Find the cells and give the type of each one.
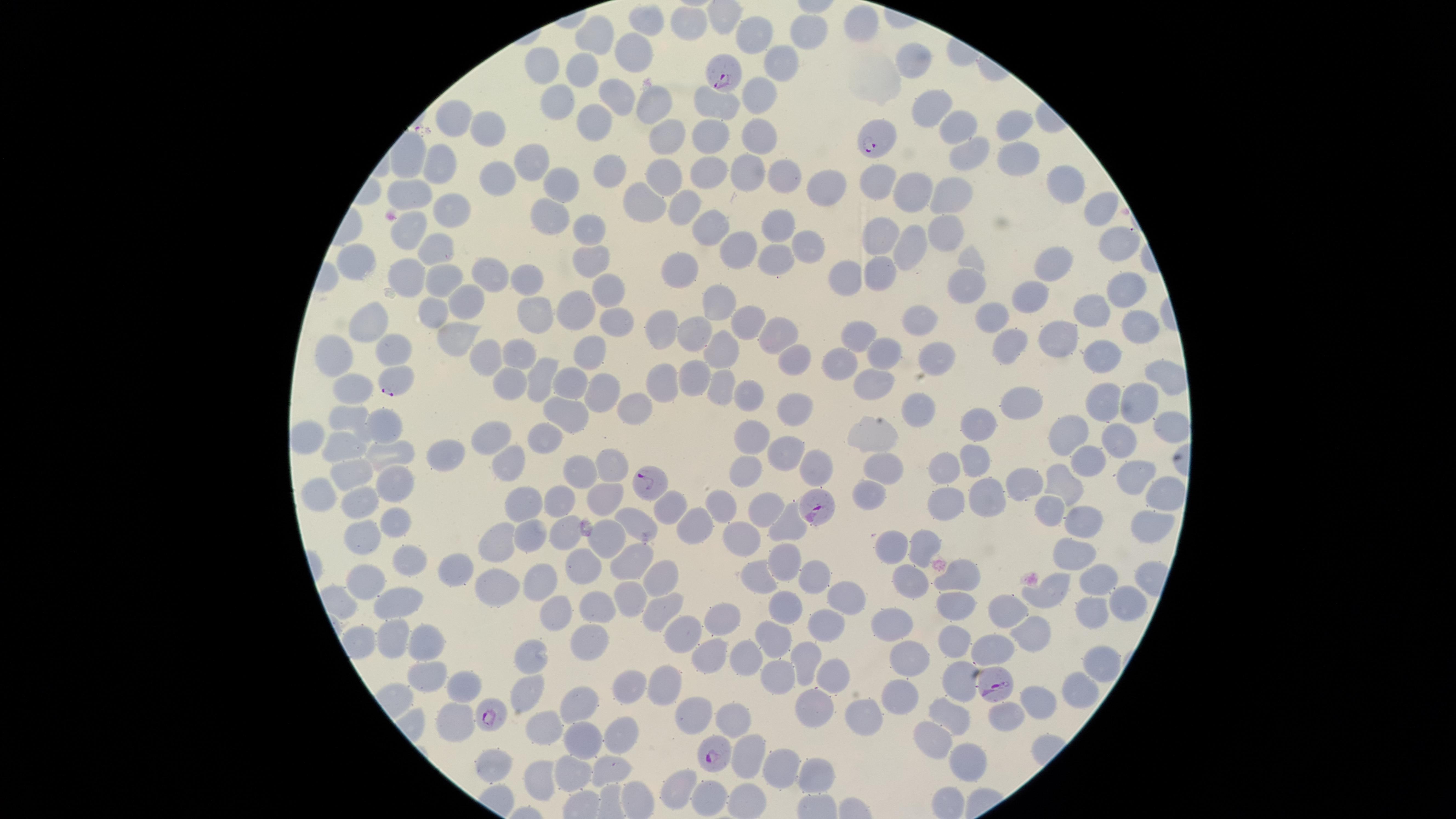

Approximate marker points, in pixels from the top-left corner.
Parasitized red blood cells: (x=728, y=77), (x=878, y=142), (x=397, y=380), (x=651, y=481), (x=812, y=506), (x=991, y=689), (x=489, y=715), (x=710, y=750).
Uninfected red blood cells: (x=646, y=23), (x=685, y=25), (x=861, y=27), (x=810, y=30), (x=755, y=32), (x=595, y=35), (x=633, y=55), (x=911, y=61), (x=779, y=65), (x=543, y=68), (x=582, y=72), (x=616, y=90), (x=756, y=92), (x=558, y=100), (x=712, y=102), (x=651, y=106), (x=926, y=108), (x=456, y=120), (x=596, y=122), (x=490, y=123), (x=958, y=129), (x=1020, y=129), (x=762, y=130), (x=665, y=132), (x=715, y=132), (x=968, y=153), (x=1019, y=156), (x=410, y=159), (x=536, y=159), (x=442, y=166), (x=611, y=167), (x=712, y=169), (x=741, y=171), (x=662, y=172), (x=781, y=172), (x=492, y=175), (x=875, y=177), (x=1058, y=181), (x=817, y=185), (x=565, y=186), (x=911, y=188), (x=413, y=192), (x=947, y=197), (x=644, y=199), (x=686, y=203), (x=1095, y=207), (x=452, y=208), (x=545, y=214), (x=588, y=224), (x=781, y=224), (x=708, y=229), (x=879, y=233), (x=410, y=234), (x=945, y=236), (x=435, y=245), (x=906, y=245), (x=740, y=248), (x=803, y=249), (x=1119, y=249), (x=586, y=256), (x=775, y=258), (x=361, y=260), (x=1054, y=262), (x=677, y=264), (x=880, y=265), (x=403, y=272), (x=441, y=273), (x=491, y=273), (x=523, y=275), (x=845, y=275), (x=962, y=285), (x=610, y=286), (x=1121, y=289), (x=1032, y=298), (x=459, y=301), (x=716, y=304), (x=1092, y=308), (x=572, y=309), (x=432, y=312), (x=536, y=316), (x=994, y=318), (x=1138, y=319), (x=619, y=320), (x=374, y=321), (x=917, y=321), (x=741, y=323), (x=695, y=330), (x=661, y=332), (x=1065, y=332), (x=775, y=333), (x=856, y=333), (x=450, y=334), (x=1009, y=340), (x=388, y=347), (x=1106, y=351), (x=715, y=352), (x=883, y=352), (x=588, y=355), (x=334, y=356), (x=482, y=357), (x=516, y=357), (x=937, y=363), (x=794, y=364), (x=841, y=365), (x=695, y=374), (x=1159, y=374), (x=666, y=376), (x=344, y=379), (x=539, y=379), (x=504, y=381), (x=570, y=381), (x=716, y=386), (x=598, y=387), (x=875, y=388), (x=747, y=390), (x=1026, y=399), (x=1106, y=400), (x=1135, y=400), (x=789, y=403), (x=632, y=408), (x=565, y=411), (x=912, y=413), (x=354, y=414), (x=979, y=419), (x=384, y=425), (x=1163, y=425), (x=1065, y=428), (x=747, y=430), (x=539, y=435), (x=874, y=435), (x=489, y=436), (x=1116, y=440), (x=338, y=444), (x=789, y=446), (x=450, y=448), (x=393, y=452), (x=1088, y=458), (x=969, y=461), (x=508, y=463), (x=884, y=468), (x=811, y=469), (x=607, y=471), (x=739, y=471), (x=940, y=471), (x=581, y=472), (x=354, y=474), (x=1128, y=479), (x=1062, y=481), (x=1022, y=482), (x=397, y=485), (x=602, y=492), (x=981, y=492), (x=320, y=493), (x=1160, y=494), (x=565, y=495), (x=864, y=495), (x=355, y=501), (x=524, y=503), (x=1053, y=503), (x=946, y=504), (x=767, y=505), (x=667, y=507), (x=717, y=507), (x=390, y=516), (x=1076, y=521), (x=694, y=524), (x=635, y=525), (x=783, y=525), (x=1149, y=526), (x=564, y=529), (x=747, y=531), (x=527, y=533), (x=355, y=538), (x=493, y=538), (x=609, y=540), (x=888, y=545), (x=919, y=546), (x=1069, y=552), (x=408, y=557), (x=783, y=557), (x=627, y=558), (x=456, y=567), (x=581, y=567), (x=908, y=572), (x=957, y=575), (x=658, y=576), (x=819, y=576), (x=535, y=577), (x=1096, y=577), (x=366, y=578), (x=761, y=578), (x=500, y=580), (x=1050, y=593), (x=629, y=597), (x=399, y=599), (x=1122, y=599), (x=842, y=600), (x=953, y=602), (x=594, y=605), (x=659, y=606), (x=1005, y=606), (x=1080, y=609), (x=779, y=610), (x=556, y=612), (x=715, y=614), (x=826, y=621), (x=890, y=626), (x=681, y=632), (x=1029, y=632), (x=391, y=635), (x=422, y=636), (x=588, y=636), (x=770, y=637), (x=955, y=639), (x=990, y=647), (x=708, y=654), (x=533, y=657), (x=802, y=657), (x=908, y=658), (x=744, y=659), (x=1094, y=664), (x=425, y=672), (x=778, y=672), (x=831, y=672), (x=461, y=681), (x=664, y=683), (x=957, y=683), (x=619, y=687), (x=896, y=691), (x=524, y=692), (x=1071, y=694), (x=1030, y=702), (x=578, y=703), (x=814, y=703), (x=690, y=712), (x=1007, y=715), (x=732, y=718), (x=863, y=718), (x=951, y=718), (x=451, y=725), (x=550, y=730), (x=618, y=730), (x=932, y=735), (x=583, y=737), (x=750, y=750), (x=492, y=760), (x=962, y=763), (x=775, y=766), (x=607, y=767), (x=811, y=770), (x=570, y=772), (x=535, y=778), (x=675, y=782), (x=706, y=797).
No white blood cells identified.

species: Plasmodium falciparum
stain: Giemsa
field_of_view: single
image_size: 1456×819 pixels
visible_region: circular
capture: smartphone photograph through the microscope eyepiece
preparation: thin smear of blood